Point out every malaria parasite.
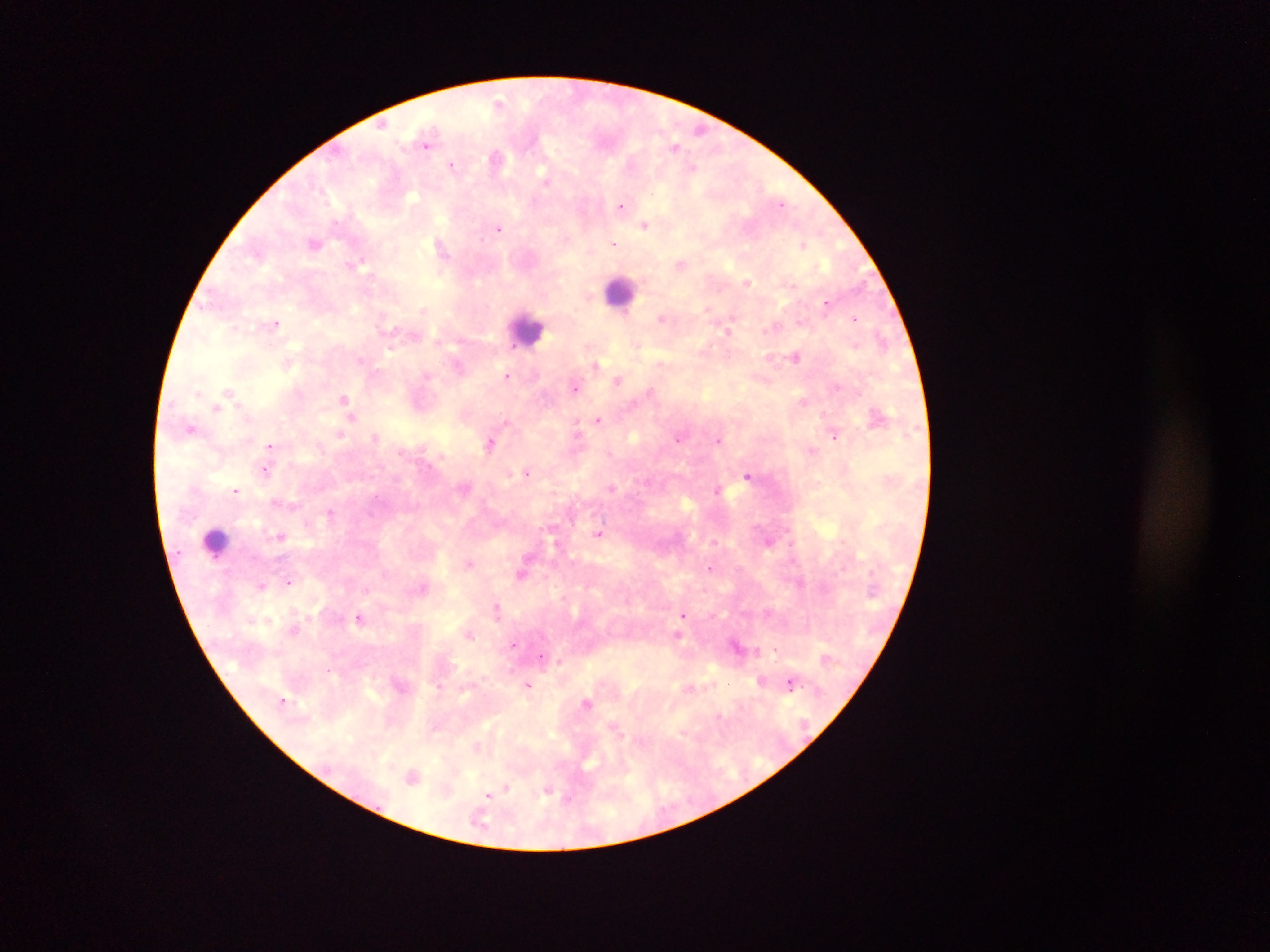

Approximate centers as x y in pixels.
Malaria parasites: 500 101; 674 145; 426 146; 452 164; 545 179; 622 207; 645 225; 499 228; 480 239; 614 243; 804 244; 441 247; 681 263; 364 264; 747 281; 423 310; 708 310; 855 319; 661 320; 281 324; 726 332; 638 344; 391 350; 797 357; 361 360; 661 363; 596 364; 506 376; 618 378; 576 387; 651 391; 231 393; 804 402; 216 409; 824 414; 877 415; 599 419; 506 421; 575 423; 191 429; 339 433; 835 436; 377 437; 678 438; 720 438; 489 444; 271 446; 812 450; 408 451; 266 471; 527 471; 748 475; 612 487; 463 488; 717 488; 235 489; 273 501; 294 506; 331 513; 280 535; 598 535; 468 562; 709 567; 521 574; 289 581; 261 585; 497 608; 685 613; 360 617; 293 630; 470 634; 678 635; 512 645; 542 656; 761 680; 789 683; 529 685; 690 687; 586 701; 478 746; 412 772; 506 788; 549 791; 488 795.

Summary:
  - Leukocyte locations: 614 295; 523 327; 216 535
  - Capture: mobile-phone photograph through a microscope
  - Image size: 1270×952 pixels
  - Field of view: single
  - Country: Ghana
  - Preparation: thick blood film